Point out each malaria parasite.
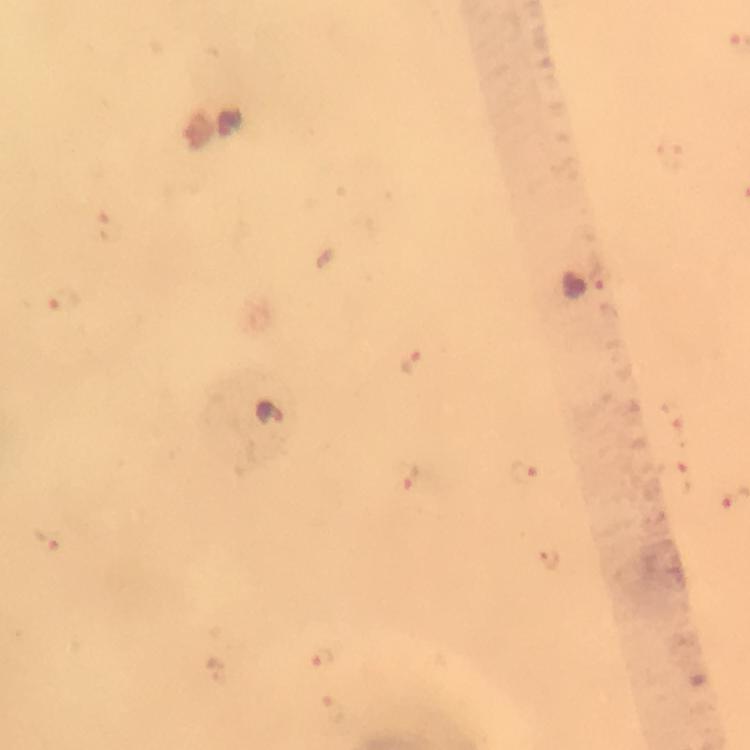
Approximate object centers, in pixels from the top-left corner.
Malaria parasites: (x=112, y=226), (x=600, y=277), (x=67, y=301), (x=412, y=363), (x=269, y=414), (x=525, y=475), (x=413, y=477), (x=676, y=482), (x=45, y=538), (x=550, y=560), (x=322, y=659), (x=218, y=670).

magnification = 100x
preparation = thick blood smear
image size = 750×750 pixels
context = from a malaria diagnostic workup
capture = smartphone photograph through a microscope
immersion oil = used
cropped from = one field of view
stain = Giemsa